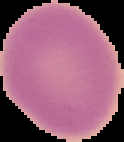 Malaria status: uninfected. The area outside the segmented cell region is set to black. From a thin blood smear. Image is 124×142 pixels.